Name the parasite shown.
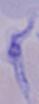

A trypanosome.

Summary:
  - Modality: micrograph
  - Magnification: 1000x